Give the position of every leukocyte visible.
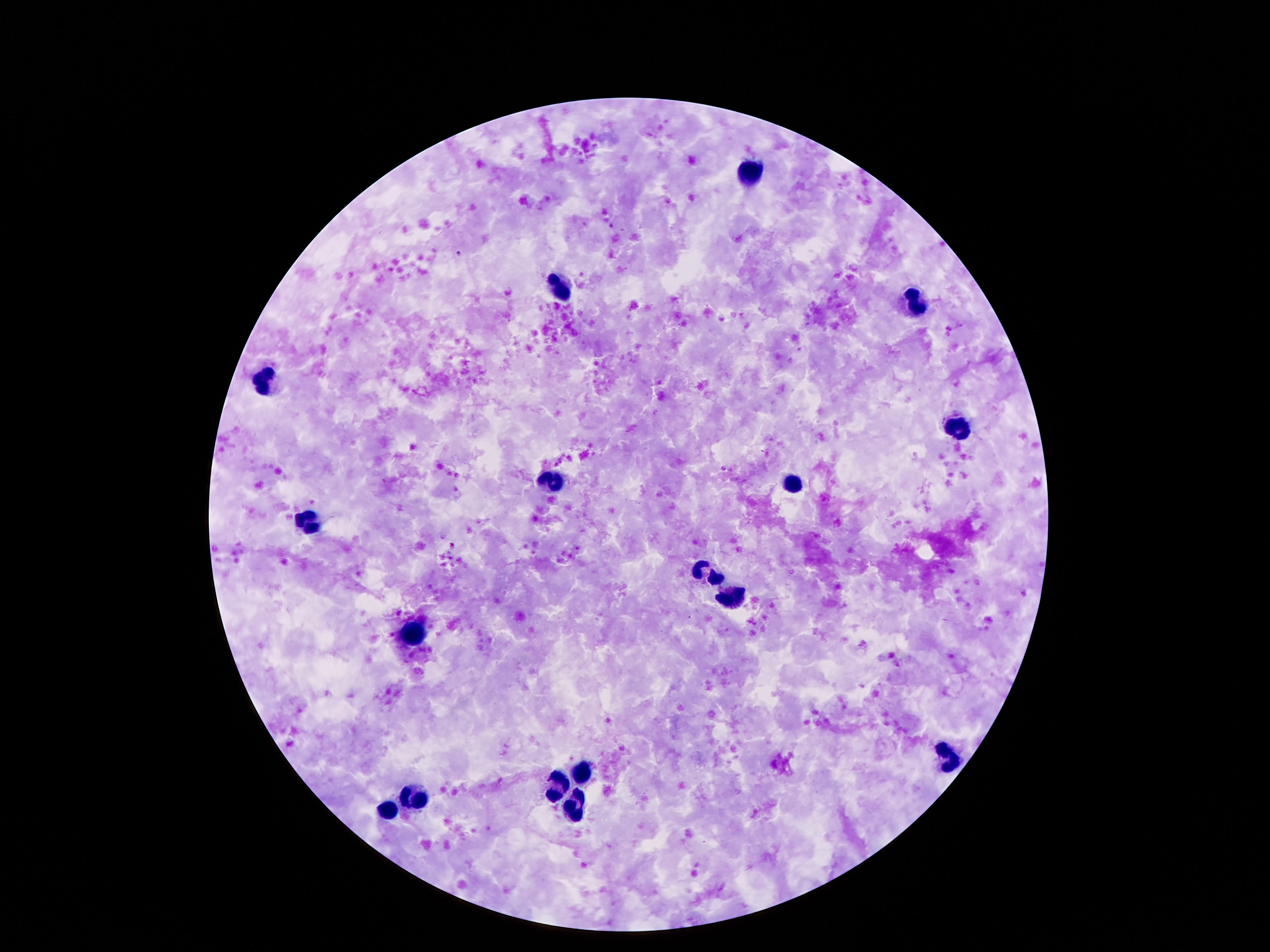

Approximate object centers, in pixels from the top-left corner.
Leukocytes: (x=751, y=170), (x=561, y=285), (x=911, y=304), (x=266, y=381), (x=961, y=431), (x=551, y=482), (x=792, y=483), (x=305, y=521), (x=704, y=572), (x=733, y=597), (x=417, y=636), (x=948, y=758), (x=579, y=773), (x=557, y=785), (x=413, y=801), (x=575, y=811), (x=387, y=813).

Summary:
  - Capture: smartphone camera through the microscope eyepiece
  - Preparation: thick blood smear
  - Image size: 1270×952 pixels
  - Field of view: single
  - Magnification: 100x
  - Patient malaria status: uninfected
  - Stain: Giemsa